Assess this cell for malaria.
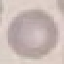
Uninfected.

Automatically extracted cell patch, resized to 64 × 64 pixels. Thin blood smear. Acquired by smartphone through the microscope eyepiece. Giemsa-stained preparation.